Classify this cell by malaria status.
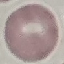
It is uninfected.

image type = automatically extracted cell patch, resized to 64 × 64 pixels
capture = smartphone camera at the microscope eyepiece
stain = Giemsa
preparation = thin blood film